Report the malaria status of this cell.
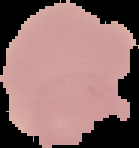
Uninfected.

image_type: segmented cell region with the area outside set to black
image_size: 139×148 pixels
preparation: thin blood smear